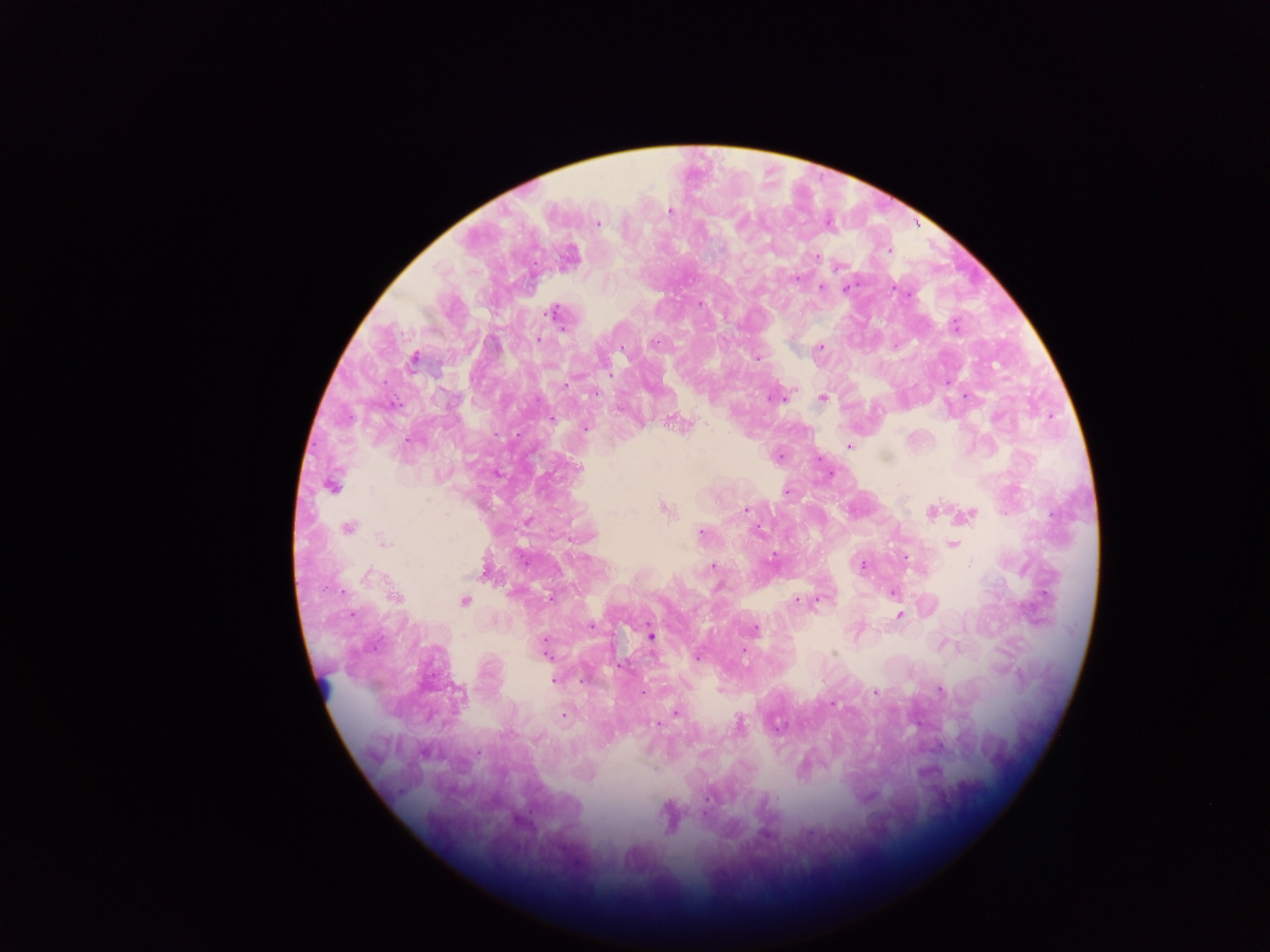

Approximate centers as (x, y) in pixels. Malaria parasite locations: (669, 210), (597, 223), (741, 223), (888, 250), (816, 256), (795, 279), (822, 288), (846, 288), (894, 288), (700, 303), (553, 313), (955, 325), (539, 339), (655, 341), (819, 347), (622, 348), (414, 358), (757, 358), (595, 393), (772, 398), (822, 398), (552, 419), (673, 422), (585, 427), (848, 445), (578, 469), (331, 485), (787, 492), (664, 508), (746, 510), (931, 511), (966, 515), (348, 527), (701, 533), (953, 545), (773, 558), (862, 564), (713, 566), (484, 574), (893, 593), (395, 597), (550, 598), (820, 600), (464, 601), (797, 601), (900, 616), (591, 627), (754, 628), (651, 636), (545, 643), (744, 652), (834, 654), (697, 657), (553, 680), (584, 680), (940, 690), (642, 692), (875, 692), (460, 695), (832, 704), (676, 713), (564, 715), (658, 724), (739, 725), (777, 727), (478, 752), (654, 769), (708, 799), (764, 834). Collected in Ghana. One field of view. Mobile-phone photograph taken through the microscope. Thick blood film. Image is 1270×952 pixels.